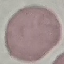
Malaria status: uninfected. Photographed with a smartphone camera at the microscope eyepiece. Automatically extracted cell patch, resized to 64 × 64 pixels. Thin smear of blood. Giemsa stain.